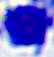

{
  "identification": "white blood cell",
  "modality": "photomicrograph",
  "magnification": "400x"
}